Name the cell type shown.
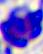
A leukocyte.

Summary:
  - Magnification: 400x
  - Modality: micrograph